Identify the parasite.
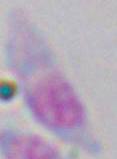
This is Toxoplasma gondii.

Summary:
  - Modality: photomicrograph
  - Magnification: 1000x